Identify the preparation type.
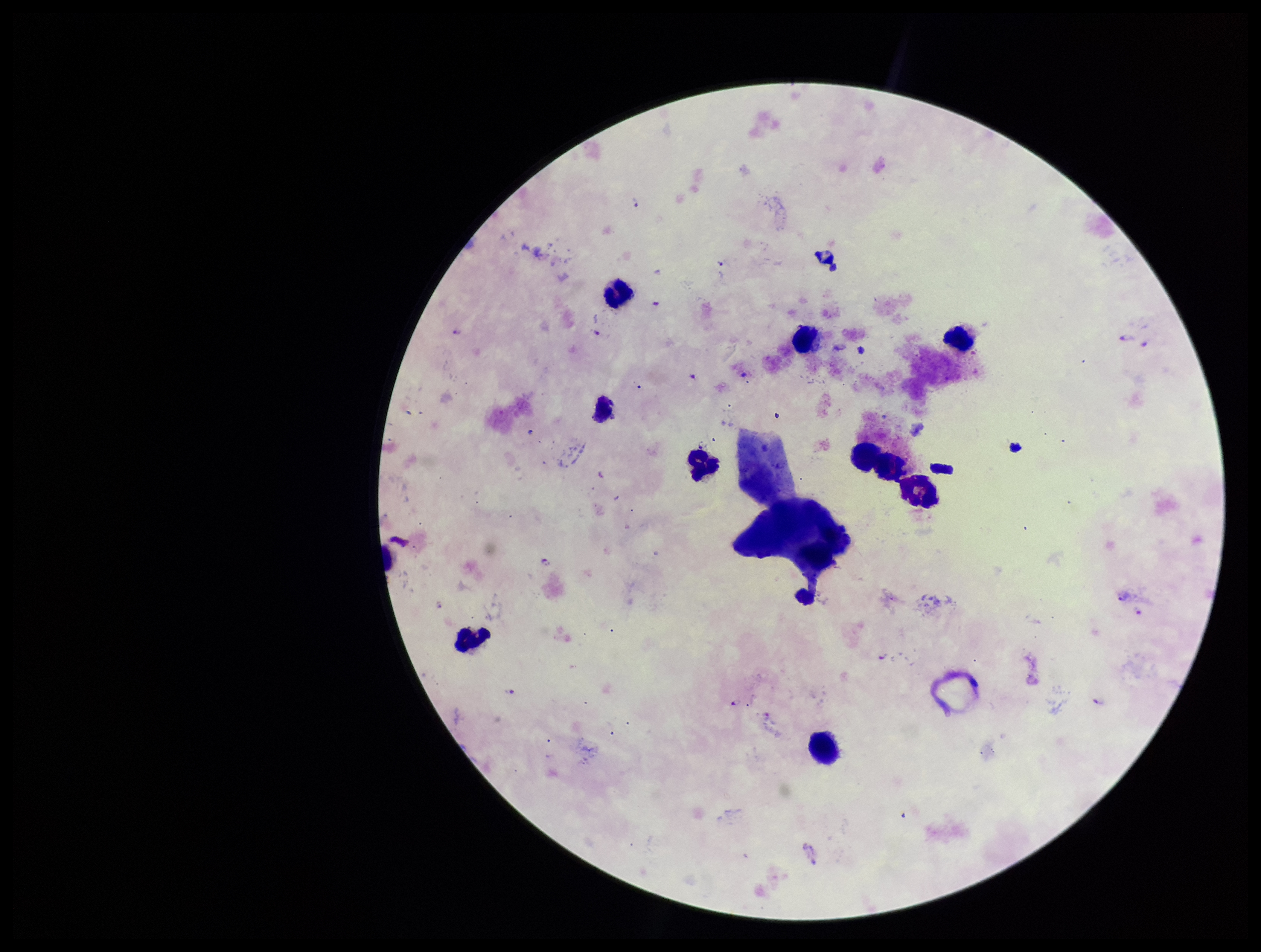
Thick.

Smartphone photograph taken through the eyepiece of a microscope. Parasite count: 3. Plasmodium parasites: seen. Species reported for this patient: Plasmodium falciparum. Image is 1261×952 pixels. Stained with Giemsa. Single field of view. Patient malaria status: positive. Leukocyte count: 10.